Give the position of every leukocyte visible.
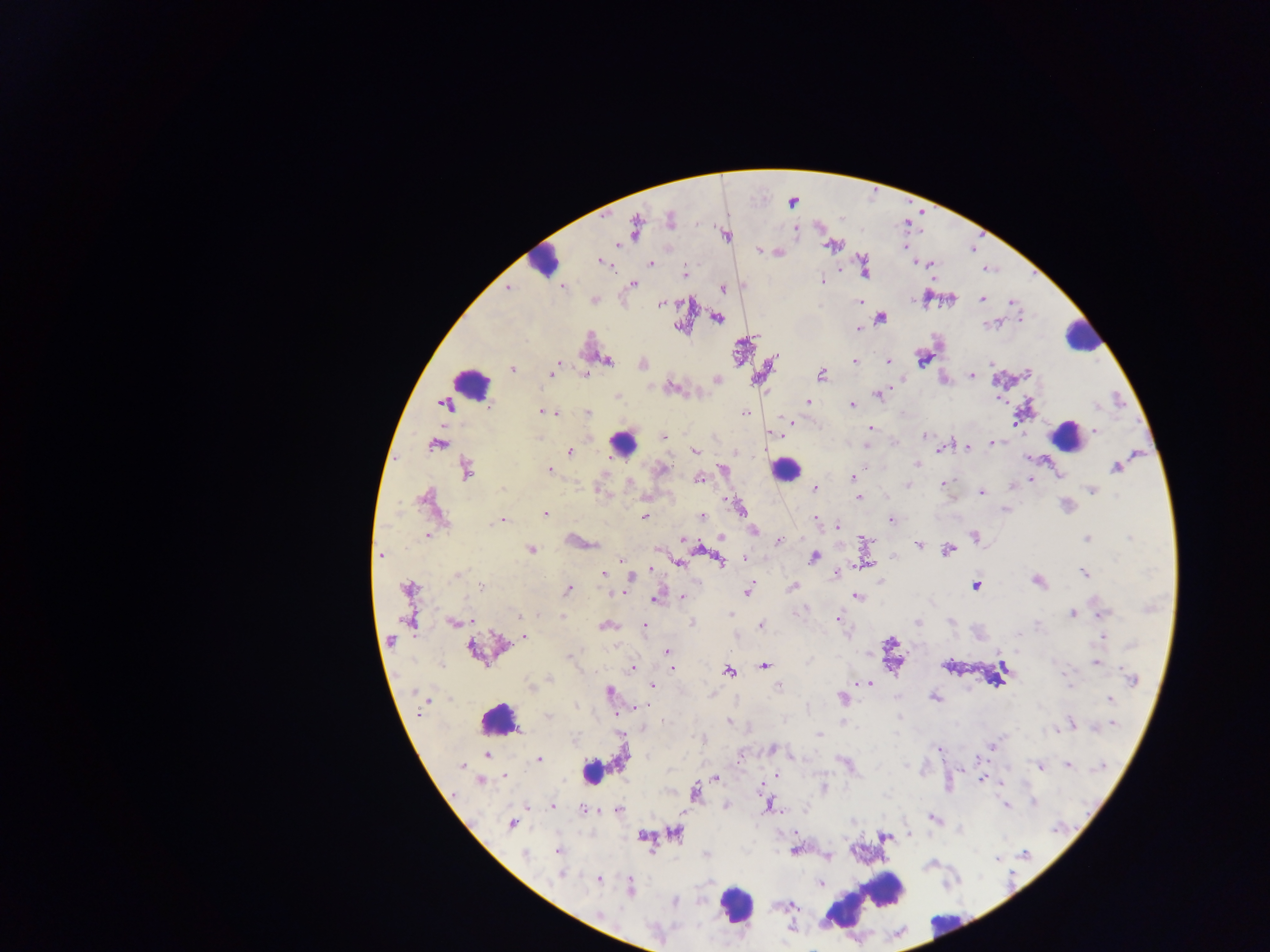
Approximate centers as [x, y] in pixels.
Leukocytes: [544, 262], [1081, 336], [470, 383], [1067, 437], [623, 442], [786, 469], [498, 720], [591, 771], [863, 902], [735, 904], [946, 922].

Malaria parasite locations: [792, 201], [671, 219], [636, 227], [796, 229], [726, 234], [618, 245], [833, 245], [759, 250], [778, 252], [917, 261], [601, 262], [650, 264], [929, 265], [864, 267], [684, 272], [820, 279], [633, 283], [562, 286], [723, 287], [507, 289], [925, 298], [950, 298], [981, 298], [593, 299], [860, 302], [1012, 302], [660, 304], [879, 316], [717, 317], [1020, 318], [994, 324], [681, 327], [858, 328], [922, 357], [606, 361], [852, 361], [887, 361], [557, 364], [642, 364], [990, 364], [511, 368], [1027, 372], [585, 373], [820, 374], [550, 375], [971, 375], [717, 379], [670, 386], [877, 394], [616, 396], [1000, 398], [807, 402], [443, 403], [853, 405], [488, 407], [543, 410], [586, 412], [555, 413], [745, 413], [790, 421], [869, 428], [1094, 431], [769, 433], [924, 435], [663, 437], [991, 443], [436, 444], [866, 445], [967, 446], [941, 448], [695, 450], [569, 452], [916, 464], [1116, 467], [662, 469], [723, 469], [549, 470], [468, 475], [1059, 475], [699, 478], [852, 478], [1030, 480], [629, 481], [941, 484], [907, 486], [1011, 487], [813, 488], [1092, 490], [980, 492], [644, 496], [859, 497], [425, 498], [1066, 505], [740, 508], [1005, 510], [545, 513], [702, 516], [643, 517], [814, 517], [891, 519], [501, 520], [838, 526], [753, 529], [428, 535], [974, 537], [720, 538], [1086, 538], [682, 539], [778, 541], [865, 541], [918, 543], [655, 548], [530, 549], [948, 550], [381, 555], [813, 556], [892, 557], [743, 558], [622, 559], [718, 559], [678, 562], [865, 565], [650, 568], [836, 572], [1085, 573], [602, 574], [456, 575], [631, 577], [1037, 580], [793, 586], [974, 586], [481, 587], [408, 588], [567, 588], [747, 589], [617, 592], [856, 596], [681, 597], [655, 599], [1072, 613], [731, 614], [840, 614], [1101, 614], [518, 615], [560, 615], [409, 617], [837, 618], [915, 621], [453, 622], [691, 623], [605, 625], [644, 625], [760, 625], [523, 637], [1101, 637], [391, 640], [614, 646], [666, 651], [1095, 662], [764, 665], [633, 668], [672, 669], [728, 670], [550, 678], [1132, 679], [852, 684], [869, 684], [651, 685], [778, 686], [609, 691], [934, 697], [843, 698], [1109, 699], [424, 702], [634, 708], [548, 716], [900, 718], [729, 721], [1069, 724], [1113, 724], [1057, 730], [820, 734], [992, 746], [939, 748], [772, 749], [487, 755], [538, 759], [1067, 764], [462, 766], [1040, 766], [777, 774], [504, 776], [715, 777], [981, 780], [998, 780], [480, 781], [760, 788], [822, 788], [694, 792], [1033, 803], [726, 804], [527, 805], [551, 805], [769, 805], [1005, 805], [583, 810], [618, 810], [933, 818], [510, 823], [675, 832], [908, 834], [885, 835], [643, 836], [558, 850], [795, 850], [524, 854], [828, 856], [560, 874], [598, 879], [821, 883], [629, 889], [776, 906], [792, 906], [791, 927]. Thick blood film. Single field of view. Sample from Ghana. Photographed through a microscope with a mobile-phone camera. Image is 1270×952 pixels.